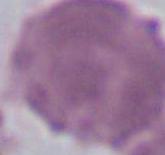

Captured at 1000x magnification. Photomicrograph. A red blood cell is shown.